Outline each blood parasite and name the species.
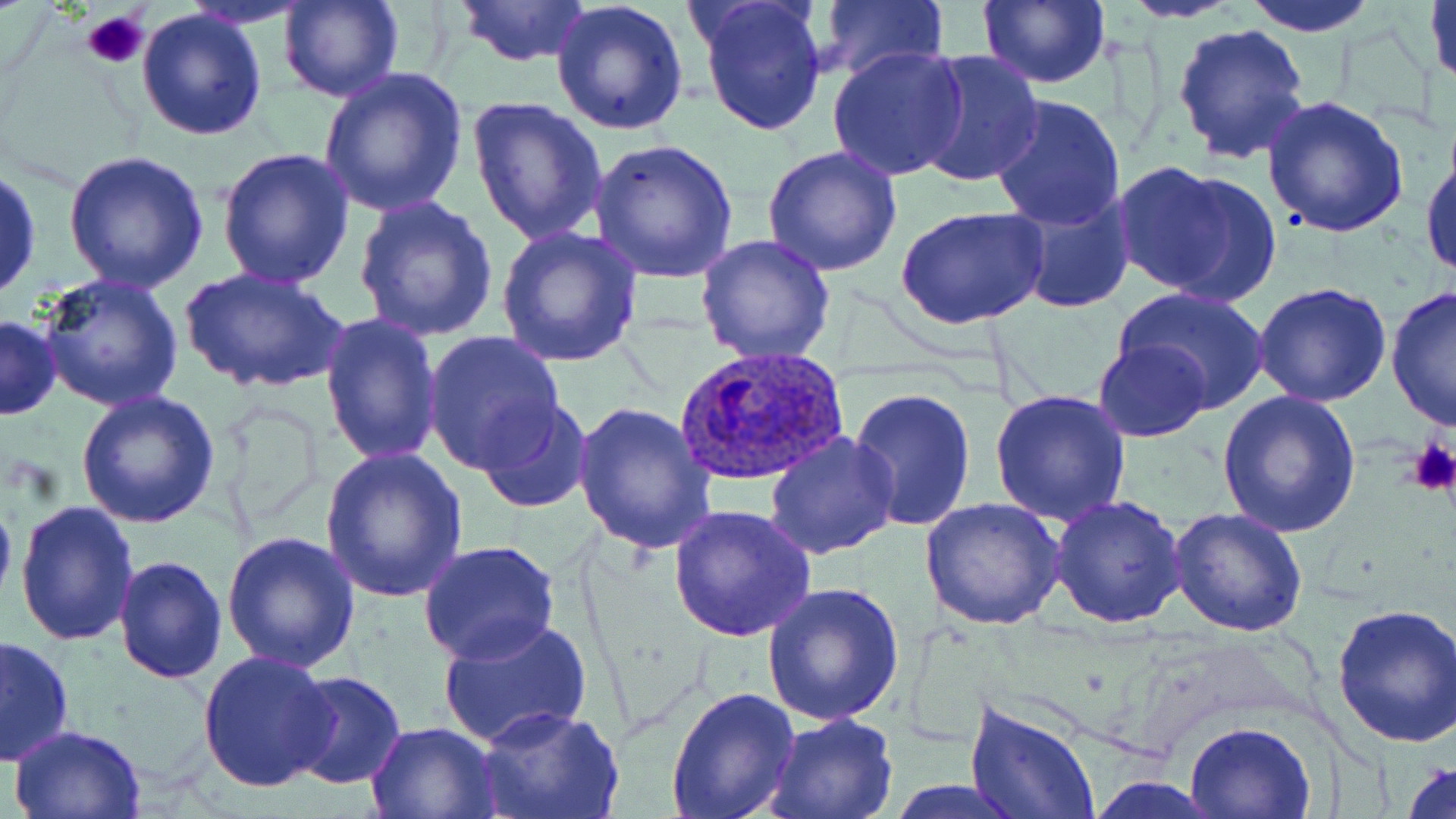

Approximate bounding boxes as named x1/y1/x2/y2 corners in pixels.
Plasmodium ovale-infected red blood cells: (x1=676, y1=347, x2=850, y2=488).
No Plasmodium falciparum, Plasmodium malariae, Plasmodium vivax, Babesia divergens, or Trypanosoma brucei observed.

Summary:
  - Platelet locations: (x1=81, y1=10, x2=150, y2=70), (x1=1407, y1=437, x2=1456, y2=495)
  - Uninfected red blood cell locations: (x1=277, y1=0, x2=403, y2=103), (x1=454, y1=0, x2=591, y2=68), (x1=694, y1=0, x2=828, y2=137), (x1=977, y1=0, x2=1110, y2=89), (x1=1119, y1=0, x2=1244, y2=22), (x1=1240, y1=0, x2=1383, y2=36), (x1=1426, y1=0, x2=1456, y2=93), (x1=817, y1=1, x2=948, y2=82), (x1=551, y1=2, x2=691, y2=137), (x1=137, y1=5, x2=269, y2=141), (x1=1171, y1=22, x2=1312, y2=166), (x1=826, y1=43, x2=970, y2=181), (x1=912, y1=50, x2=1045, y2=189), (x1=317, y1=67, x2=467, y2=217), (x1=988, y1=93, x2=1130, y2=230), (x1=1259, y1=93, x2=1409, y2=238), (x1=466, y1=94, x2=608, y2=246), (x1=588, y1=138, x2=741, y2=282), (x1=1421, y1=142, x2=1455, y2=282), (x1=216, y1=147, x2=355, y2=290), (x1=762, y1=147, x2=903, y2=280), (x1=60, y1=149, x2=209, y2=294), (x1=1111, y1=162, x2=1272, y2=303), (x1=0, y1=164, x2=42, y2=304), (x1=1009, y1=188, x2=1138, y2=314), (x1=353, y1=197, x2=499, y2=343), (x1=897, y1=206, x2=1049, y2=332), (x1=494, y1=224, x2=643, y2=367), (x1=696, y1=235, x2=835, y2=365), (x1=178, y1=266, x2=348, y2=396), (x1=35, y1=271, x2=186, y2=413), (x1=1252, y1=283, x2=1392, y2=407), (x1=1113, y1=286, x2=1270, y2=412), (x1=1384, y1=287, x2=1455, y2=432), (x1=319, y1=311, x2=444, y2=467), (x1=1, y1=314, x2=62, y2=420), (x1=423, y1=329, x2=567, y2=474), (x1=1093, y1=338, x2=1212, y2=441), (x1=847, y1=385, x2=979, y2=533), (x1=988, y1=387, x2=1134, y2=526), (x1=75, y1=389, x2=222, y2=528), (x1=1217, y1=390, x2=1361, y2=537), (x1=477, y1=399, x2=593, y2=515), (x1=570, y1=401, x2=717, y2=553), (x1=764, y1=432, x2=900, y2=560), (x1=317, y1=448, x2=465, y2=602), (x1=0, y1=480, x2=17, y2=618), (x1=1048, y1=496, x2=1186, y2=628), (x1=920, y1=497, x2=1065, y2=630), (x1=14, y1=500, x2=139, y2=647), (x1=667, y1=504, x2=817, y2=641), (x1=1167, y1=508, x2=1308, y2=637), (x1=221, y1=529, x2=361, y2=672), (x1=420, y1=540, x2=560, y2=665), (x1=113, y1=554, x2=228, y2=684), (x1=763, y1=582, x2=902, y2=726), (x1=1331, y1=600, x2=1456, y2=748), (x1=437, y1=615, x2=592, y2=749), (x1=0, y1=633, x2=74, y2=766), (x1=198, y1=652, x2=339, y2=794), (x1=286, y1=670, x2=406, y2=790), (x1=664, y1=683, x2=800, y2=819), (x1=966, y1=697, x2=1100, y2=819), (x1=479, y1=708, x2=623, y2=819), (x1=762, y1=713, x2=899, y2=819), (x1=365, y1=720, x2=500, y2=817), (x1=1185, y1=720, x2=1316, y2=818), (x1=10, y1=723, x2=149, y2=817), (x1=1400, y1=757, x2=1456, y2=819), (x1=1088, y1=777, x2=1223, y2=816)
  - Slide-level diagnosis: Plasmodium ovale
  - Preparation: thin blood film
  - Field of view: single
  - Stain: May-Grünwald-Giemsa
  - Image size: 1456×819 pixels
  - Magnification: 1000x
  - Modality: light microscopy